Classify this cell by malaria status.
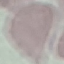
Uninfected.

image type = cell patch, automatically extracted from a larger field of view and resized to 64 × 64 pixels
stain = Giemsa
capture = smartphone camera at the microscope eyepiece
preparation = thin blood film